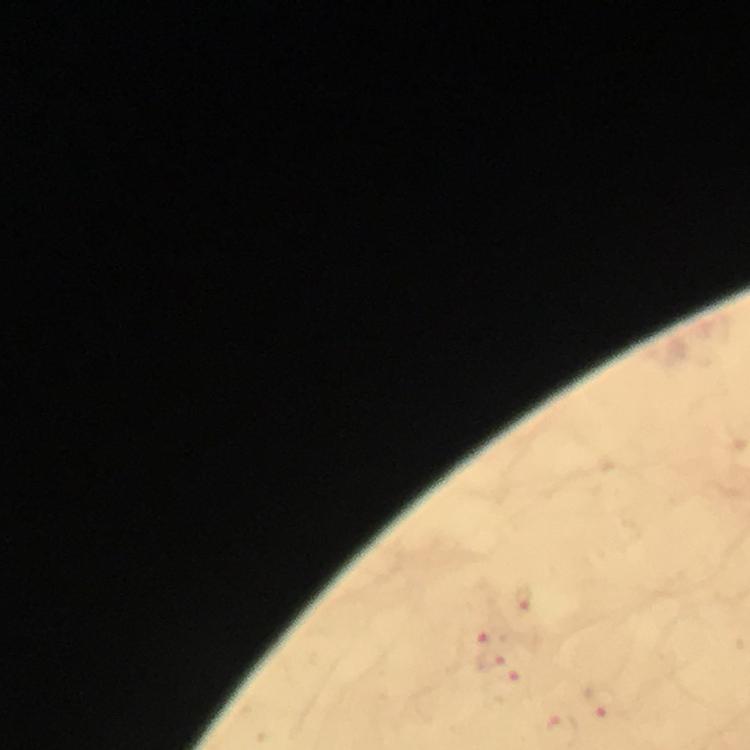
Approximate centers as [x, y] in pixels. Malaria parasite locations: [524, 602], [475, 636], [489, 658], [506, 680], [604, 702]. From a malaria diagnostic workup. Immersion oil was used. Thick smear. Cropped region of a single field of view. Giemsa stain. Photographed through the microscope with a smartphone camera. Image is 750×750 pixels. At 100x magnification.